Classify this cell by malaria status.
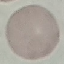
It is uninfected.

Summary:
  - Stain: Giemsa
  - Image type: automatically extracted cell patch, resized to 64 × 64 pixels
  - Capture: smartphone through the microscope eyepiece
  - Preparation: thin smear